Identify the parasite.
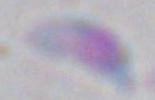

This is Toxoplasma gondii.

modality = photomicrograph
magnification = 1000x